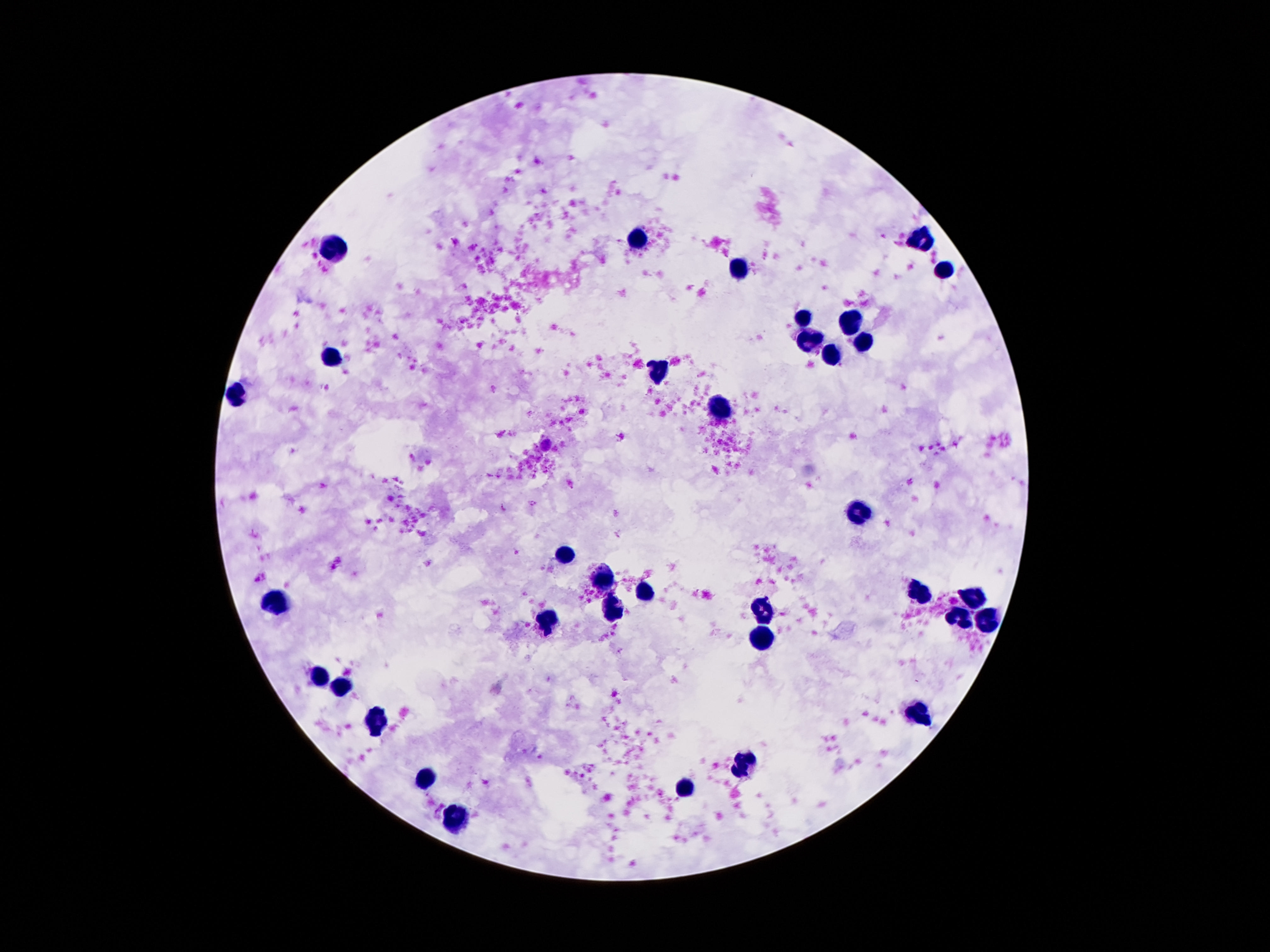

Approximate centers as [x, y] in pixels. Leukocyte locations: [638, 239], [922, 239], [334, 249], [737, 268], [943, 272], [804, 319], [854, 323], [810, 337], [861, 342], [334, 357], [833, 357], [661, 369], [235, 396], [718, 410], [859, 512], [565, 554], [604, 580], [646, 592], [919, 592], [972, 598], [277, 605], [762, 609], [613, 613], [961, 617], [550, 619], [991, 621], [758, 634], [319, 674], [344, 688], [919, 713], [376, 718], [747, 764], [428, 779], [686, 787], [456, 818]. 100x magnification. Image is 1270×952 pixels. Thick blood film. Photographed through the microscope eyepiece with a smartphone camera. Patient malaria status: uninfected. Giemsa-stained preparation. Single field of view.